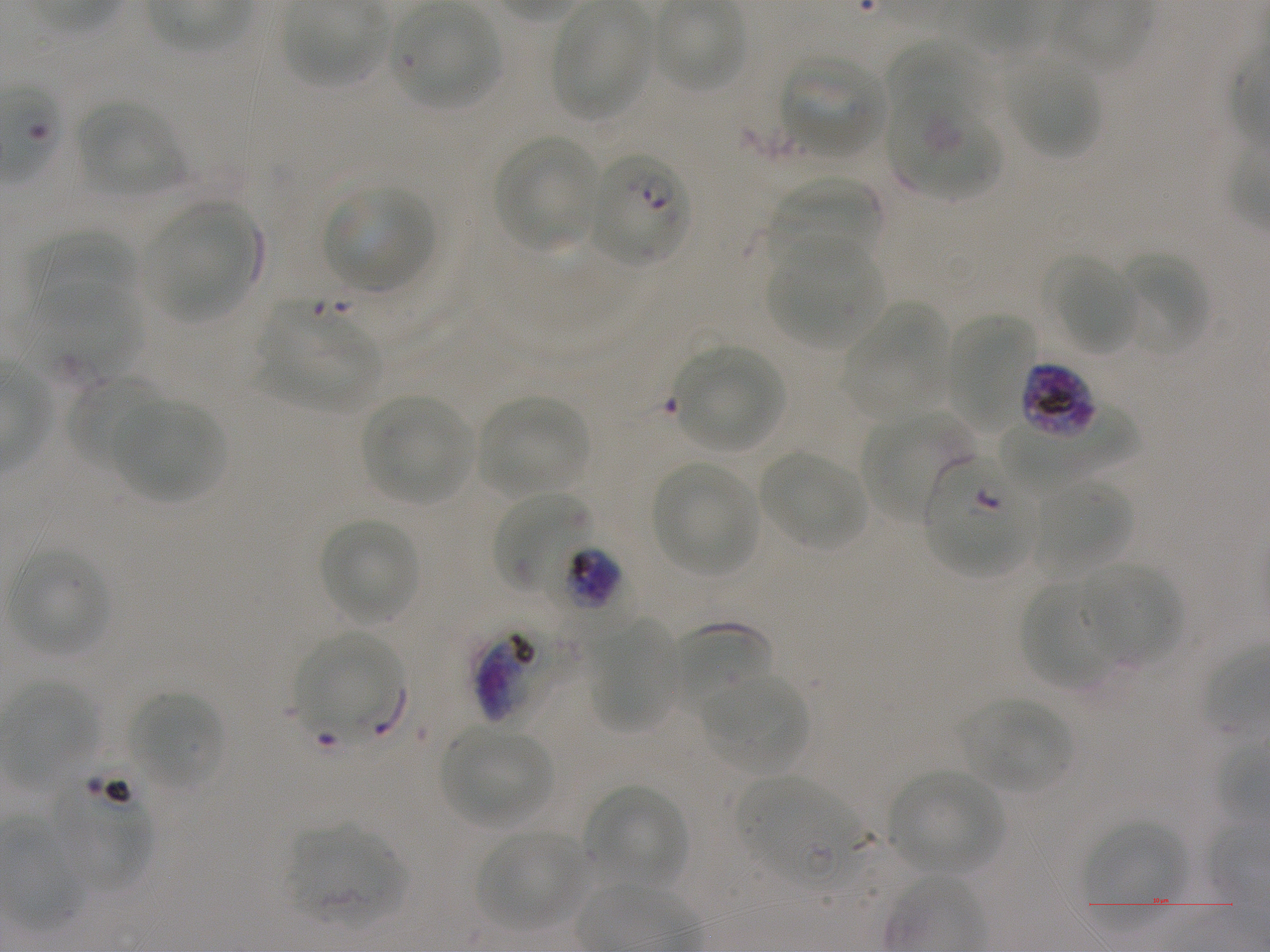

Not every red blood cell is marked. A life-cycle stage — or a range of stages, where the recorded stages span more than one — follows each staged infected red blood cell.
culture = static in-vitro Plasmodium falciparum strain NF54
life-cycle stages observed = ring, trophozoite, schizont
donor blood group = A+
locations of red blood cells of indeterminate infection status = approximate bounding boxes as {x1, y1, x2, y2} in pixels: {924, 452, 1037, 576}, {43, 755, 155, 890}, {741, 778, 864, 888}
locations of infected red blood cells = approximate bounding boxes as {x1, y1, x2, y2} in pixels: {586, 151, 690, 267} ring; {1020, 362, 1099, 439} schizont; {550, 546, 641, 632} late trophozoite to early schizont; {474, 609, 577, 721} trophozoite
field of view = one from this slide
objective = 100x, oil immersion, numerical aperture 1.25
preparation = thin blood film
stain = Giemsa
locations of uninfected red blood cells = approximate bounding boxes as {x1, y1, x2, y2} in pixels: {653, 2, 746, 91}, {391, 4, 502, 108}, {550, 5, 652, 120}, {886, 37, 979, 119}, {778, 54, 887, 158}, {1006, 57, 1102, 158}, {887, 88, 1001, 199}, {78, 100, 182, 196}, {493, 135, 601, 252}, {771, 176, 882, 268}, {322, 185, 435, 292}, {150, 204, 259, 317}, {30, 232, 137, 316}, {769, 239, 884, 349}, {1118, 251, 1208, 355}, {1052, 256, 1138, 354}, {23, 282, 146, 382}, {258, 302, 383, 411}, {841, 303, 950, 417}, {947, 312, 1035, 426}, {675, 345, 785, 450}, {68, 374, 162, 470}, {361, 394, 473, 503}, {480, 396, 587, 497}, {113, 398, 227, 502}, {863, 410, 976, 526}, {994, 415, 1138, 496}, {759, 451, 866, 550}, {652, 462, 759, 577}, {1033, 480, 1132, 576}, {494, 492, 600, 601}, {319, 517, 420, 623}, {9, 549, 111, 656}, {1082, 562, 1182, 664}, {1021, 577, 1120, 690}, {590, 623, 681, 731}, {667, 623, 772, 715}, {296, 632, 401, 733}, {702, 675, 810, 773}, {3, 683, 101, 783}, {127, 690, 224, 790}, {962, 698, 1071, 792}, {442, 727, 551, 827}, {889, 769, 1005, 875}, {585, 784, 689, 890}, {1084, 819, 1186, 907}, {287, 824, 404, 925}, {477, 831, 585, 930}
image size = 1270×952 pixels